Assess the morphology of the erythrocytes.
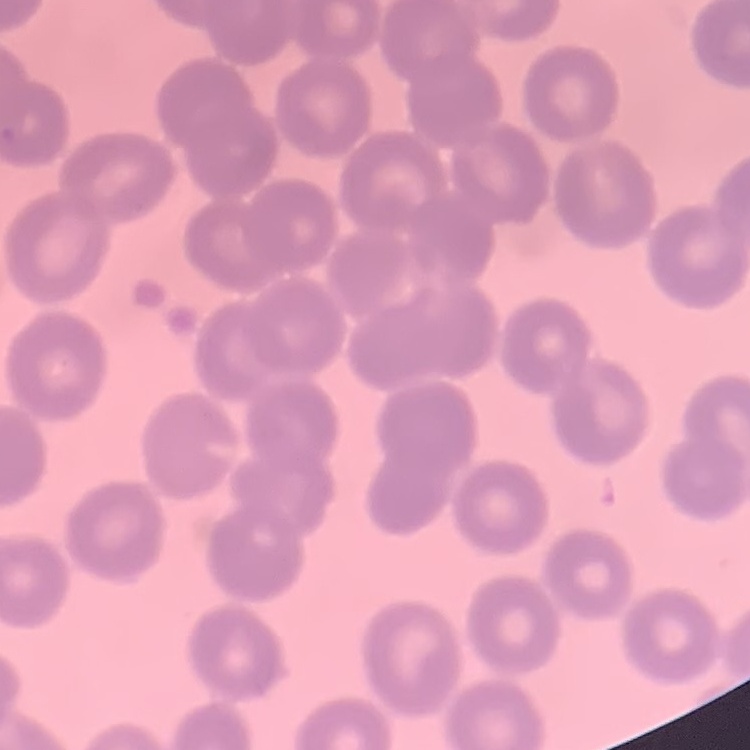

No rouleaux formation.

Summary:
  - Preparation: thin peripheral smear
  - Image type: one tile cut from a larger photomicrograph
  - Stain: Field's or Giemsa